Assess this cell for malaria.
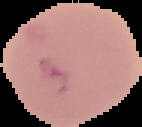
Uninfected.

Cell region segmented out of the field of view; the surrounding area is masked to black. Image is 142×127 pixels. From a thin blood smear.